Describe the morphology of the erythrocytes.
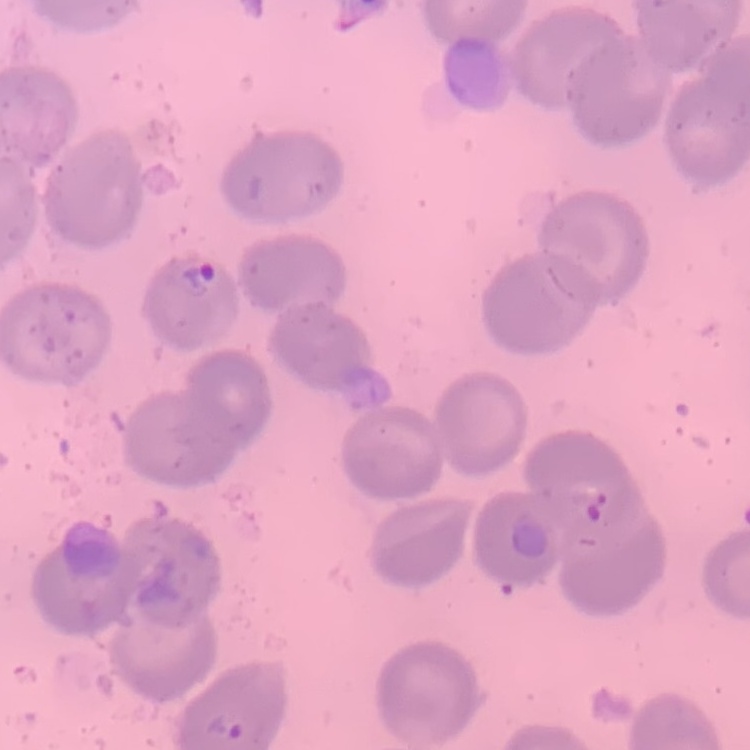

No rouleaux formation.

Square crop of a larger photomicrograph. Stained with either Field's or Giemsa. Thin blood film.